Describe the morphology of the erythrocytes.
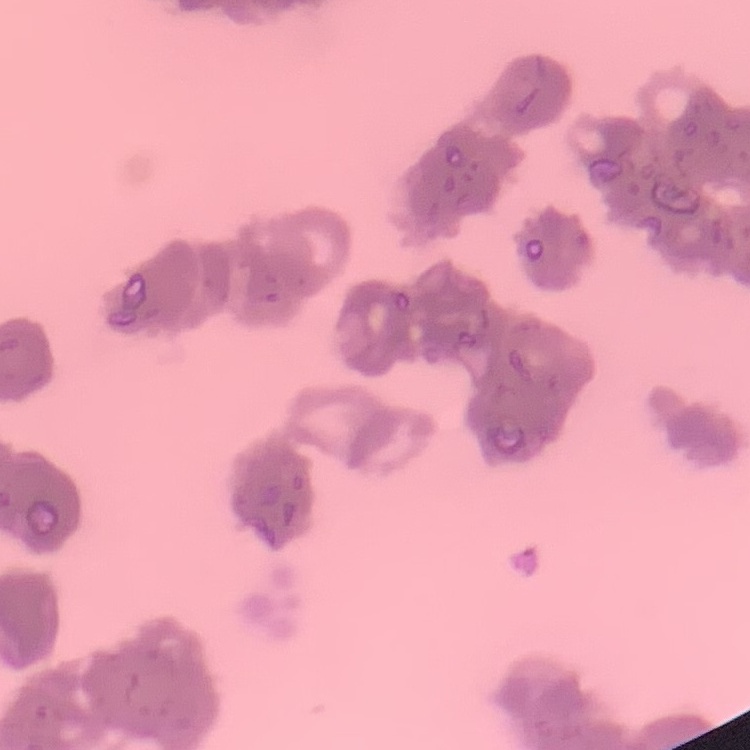

They show rouleaux formation.

One tile cut from a larger photomicrograph. Thin peripheral smear. Field's or Giemsa stain.